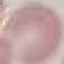
result = no malaria parasites detected
preparation = thin smear
capture = smartphone camera at the microscope eyepiece
image type = cell patch, automatically extracted from a larger field of view and resized to 64 × 64 pixels
stain = Giemsa